Report the malaria status of this cell.
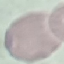
Uninfected.

capture = smartphone through the microscope eyepiece
stain = Giemsa
image type = cell patch, automatically extracted from a larger field of view and resized to 64 × 64 pixels
preparation = thin blood film